Locate every malaria parasite.
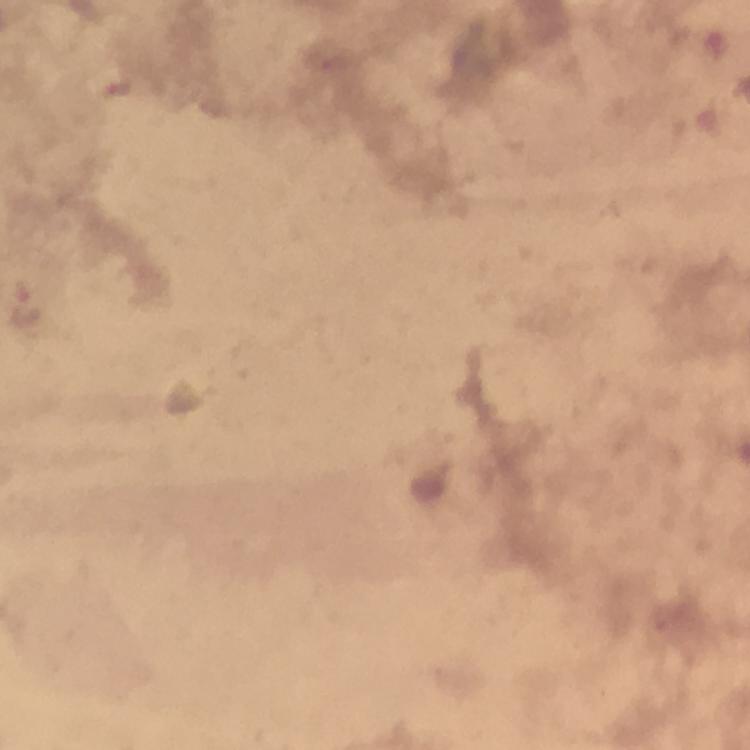
Approximate centers as {x, y} in pixels.
Malaria parasites: {25, 308}.

capture = smartphone camera through the microscope
image size = 750×750 pixels
stain = Giemsa
cropped from = a single field of view
context = from a malaria diagnostic workup
preparation = thick blood film
magnification = 100x
immersion oil = applied